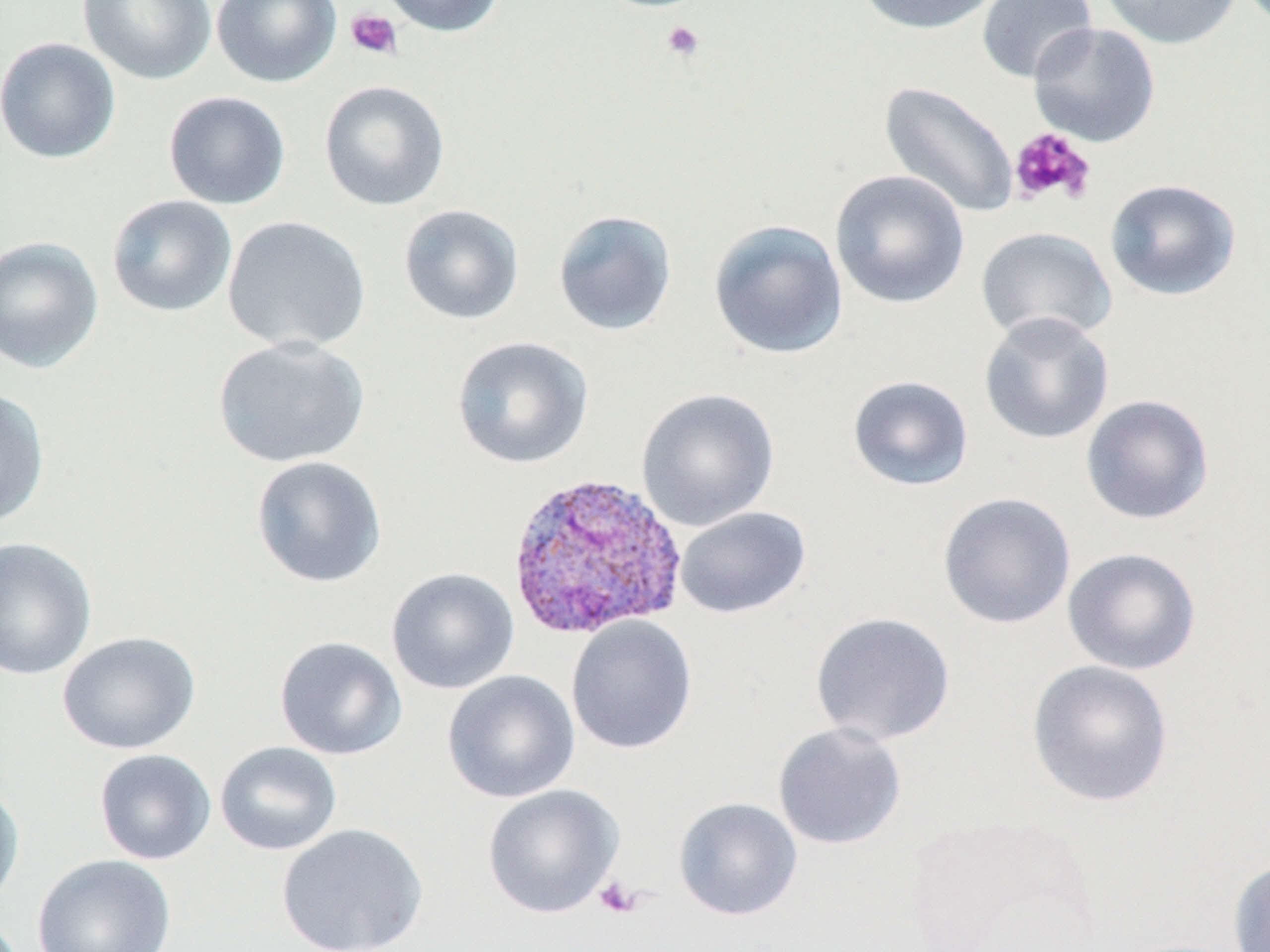
slide_level_diagnosis: Plasmodium vivax
image_size: 1270×952 pixels
magnification: 1000x
field_of_view: single
modality: light microscopy
plasmodium_vivax_infected_red_blood_cell_locations: 'approximate bounding boxes as named x1/y1/x2/y2 corners in pixels: (x1=504, y1=469, x2=687, y2=641)'
platelet_locations: 'approximate bounding boxes as named x1/y1/x2/y2 corners in pixels: (x1=345, y1=9, x2=403, y2=60), (x1=660, y1=19, x2=705, y2=63), (x1=1008, y1=127, x2=1096, y2=206), (x1=595, y1=876, x2=643, y2=918)'
preparation: thin blood smear
uninfected_red_blood_cell_locations: 'approximate bounding boxes as named x1/y1/x2/y2 corners in pixels: (x1=78, y1=0, x2=216, y2=85), (x1=211, y1=0, x2=342, y2=88), (x1=376, y1=0, x2=506, y2=37), (x1=852, y1=0, x2=1003, y2=35), (x1=1099, y1=0, x2=1242, y2=50), (x1=977, y1=1, x2=1097, y2=84), (x1=1027, y1=21, x2=1161, y2=147), (x1=0, y1=37, x2=121, y2=164), (x1=319, y1=79, x2=450, y2=211), (x1=878, y1=81, x2=1020, y2=219), (x1=163, y1=91, x2=291, y2=210), (x1=829, y1=170, x2=971, y2=310), (x1=1104, y1=178, x2=1242, y2=301), (x1=106, y1=195, x2=238, y2=318), (x1=398, y1=204, x2=524, y2=325), (x1=552, y1=209, x2=678, y2=336), (x1=222, y1=216, x2=371, y2=353), (x1=708, y1=219, x2=849, y2=360), (x1=976, y1=226, x2=1116, y2=346), (x1=0, y1=235, x2=104, y2=375), (x1=978, y1=312, x2=1115, y2=445), (x1=212, y1=335, x2=370, y2=469), (x1=451, y1=335, x2=594, y2=470), (x1=846, y1=374, x2=974, y2=491), (x1=0, y1=387, x2=50, y2=529), (x1=636, y1=387, x2=780, y2=532), (x1=1080, y1=394, x2=1215, y2=525), (x1=251, y1=455, x2=387, y2=588), (x1=937, y1=491, x2=1076, y2=629), (x1=674, y1=506, x2=811, y2=619), (x1=0, y1=536, x2=98, y2=681), (x1=1062, y1=547, x2=1202, y2=675), (x1=386, y1=567, x2=520, y2=694), (x1=809, y1=611, x2=956, y2=746), (x1=565, y1=615, x2=698, y2=755), (x1=57, y1=631, x2=201, y2=755), (x1=274, y1=635, x2=407, y2=760), (x1=1026, y1=659, x2=1174, y2=808), (x1=443, y1=670, x2=580, y2=803), (x1=773, y1=721, x2=907, y2=850), (x1=214, y1=741, x2=342, y2=856), (x1=94, y1=749, x2=216, y2=865), (x1=0, y1=779, x2=25, y2=912), (x1=482, y1=784, x2=624, y2=919), (x1=673, y1=796, x2=803, y2=920), (x1=276, y1=823, x2=428, y2=952), (x1=32, y1=853, x2=176, y2=951), (x1=1226, y1=856, x2=1270, y2=952)'
stain: May-Grünwald-Giemsa